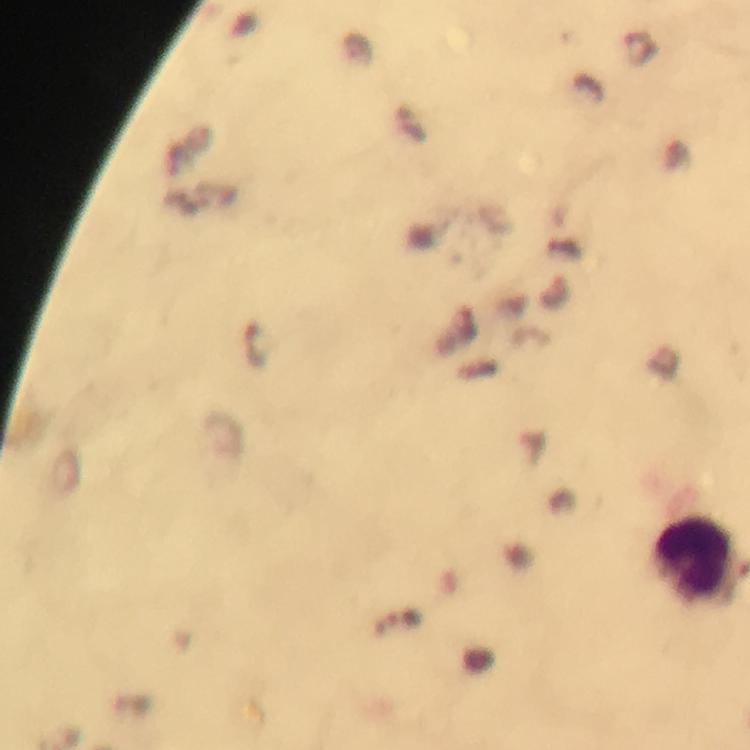
Approximate centers as (x, y) in pixels.
Summary:
  - Leukocyte locations: (696, 557)
  - Stain: Giemsa
  - Image size: 750×750 pixels
  - Preparation: thick blood film
  - Cropped from: a single field of view
  - Capture: smartphone camera through the microscope
  - Malaria parasites: none seen
  - Context: from a malaria diagnostic workup
  - Immersion oil: used
  - Magnification: 100x